Comment on the morphology of the erythrocytes.
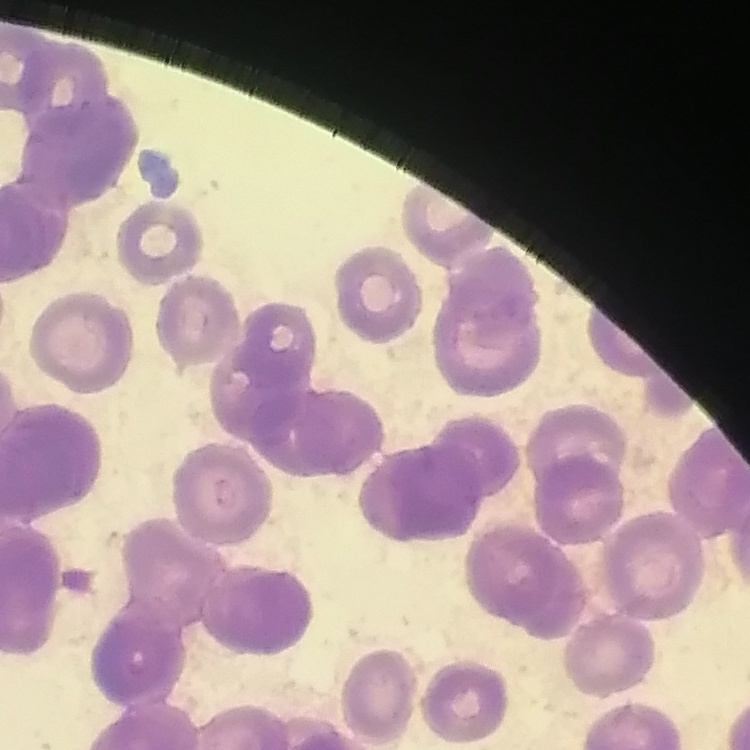

They show rouleaux formation.

image type = square crop of a larger photomicrograph
stain = Field's or Giemsa
preparation = thin blood film